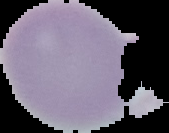 From a thin blood film. Segmented cell region on a black background. Malaria status: uninfected. Image is 169×133 pixels.